Locate every blood parasite and identify its species.
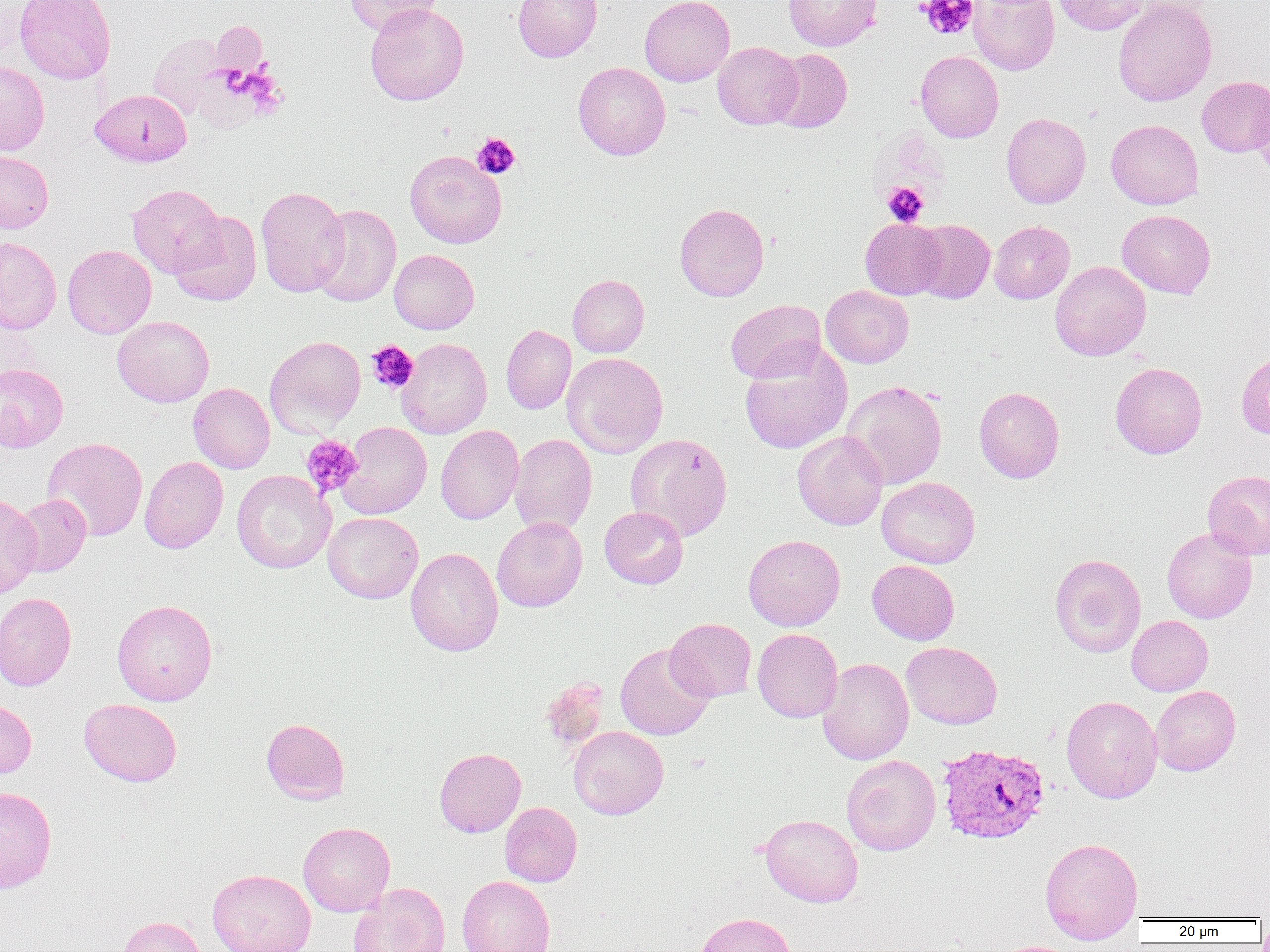

Approximate bounding boxes as (x1, y1, x2, y2) in pixels.
Plasmodium vivax-infected red blood cells: (936, 742, 1050, 845).
No Plasmodium falciparum, Plasmodium ovale, Plasmodium malariae, Babesia divergens, or Trypanosoma brucei observed.

Summary:
  - Uninfected red blood cell locations: (15, 0, 116, 84), (345, 0, 441, 36), (513, 0, 602, 62), (640, 0, 735, 86), (783, 0, 882, 51), (1053, 0, 1150, 35), (1113, 0, 1217, 107), (968, 1, 1059, 76), (364, 3, 469, 106), (211, 21, 268, 78), (148, 32, 228, 119), (713, 41, 803, 129), (769, 48, 852, 133), (916, 50, 1003, 142), (0, 62, 49, 156), (573, 62, 670, 160), (1196, 76, 1270, 157), (1251, 83, 1270, 182), (90, 89, 192, 167), (1001, 113, 1091, 208), (1106, 120, 1203, 209), (405, 150, 506, 249), (0, 151, 53, 232), (127, 184, 225, 277), (255, 186, 350, 297), (674, 203, 769, 301), (311, 204, 401, 307), (1117, 209, 1215, 298), (167, 210, 261, 306), (860, 217, 946, 299), (911, 219, 995, 304), (989, 220, 1074, 304), (0, 236, 62, 334), (62, 244, 156, 339), (390, 249, 479, 334), (1050, 261, 1151, 360), (568, 274, 649, 357), (821, 285, 914, 368), (725, 300, 826, 384), (112, 316, 214, 407), (501, 324, 576, 414), (265, 335, 366, 437), (397, 337, 492, 439), (740, 345, 852, 455), (1235, 349, 1270, 440), (562, 352, 668, 458), (1110, 362, 1207, 458), (0, 363, 68, 452), (842, 379, 947, 490), (188, 383, 275, 474), (974, 386, 1064, 483), (337, 421, 432, 519), (435, 425, 524, 524), (792, 431, 888, 530), (510, 433, 597, 535), (625, 433, 733, 541), (42, 437, 148, 541), (140, 456, 228, 554), (231, 470, 335, 574), (1202, 470, 1270, 559), (876, 477, 980, 569), (0, 493, 42, 598), (12, 494, 91, 576), (599, 506, 688, 589), (323, 512, 423, 603), (492, 517, 587, 612), (1161, 527, 1257, 624), (743, 534, 845, 631), (405, 547, 503, 656), (1050, 553, 1146, 657), (867, 560, 959, 645), (0, 593, 77, 691), (112, 599, 218, 705), (1126, 616, 1213, 695), (664, 618, 757, 702), (752, 628, 843, 722), (901, 641, 1002, 729), (615, 643, 714, 741), (817, 657, 914, 765), (540, 677, 610, 753), (1151, 685, 1241, 775), (1061, 695, 1162, 803), (79, 698, 182, 787), (0, 699, 36, 779), (261, 718, 349, 804), (568, 725, 668, 819), (434, 747, 526, 837), (842, 754, 940, 856), (0, 786, 57, 893), (499, 802, 582, 887), (760, 813, 863, 907), (298, 822, 395, 916), (1040, 837, 1143, 943), (207, 868, 316, 952), (457, 875, 554, 952), (349, 882, 451, 952), (694, 912, 796, 952), (118, 916, 207, 952), (991, 940, 1086, 952)
  - Platelet locations: (918, 0, 978, 40), (211, 22, 267, 76), (472, 133, 520, 178), (882, 182, 929, 226), (366, 339, 418, 394), (301, 435, 363, 498)
  - Slide-level diagnosis: Plasmodium vivax
  - Modality: light microscopy
  - Field of view: single
  - Magnification: 1000x
  - Image size: 1270×952 pixels
  - Preparation: thin blood smear